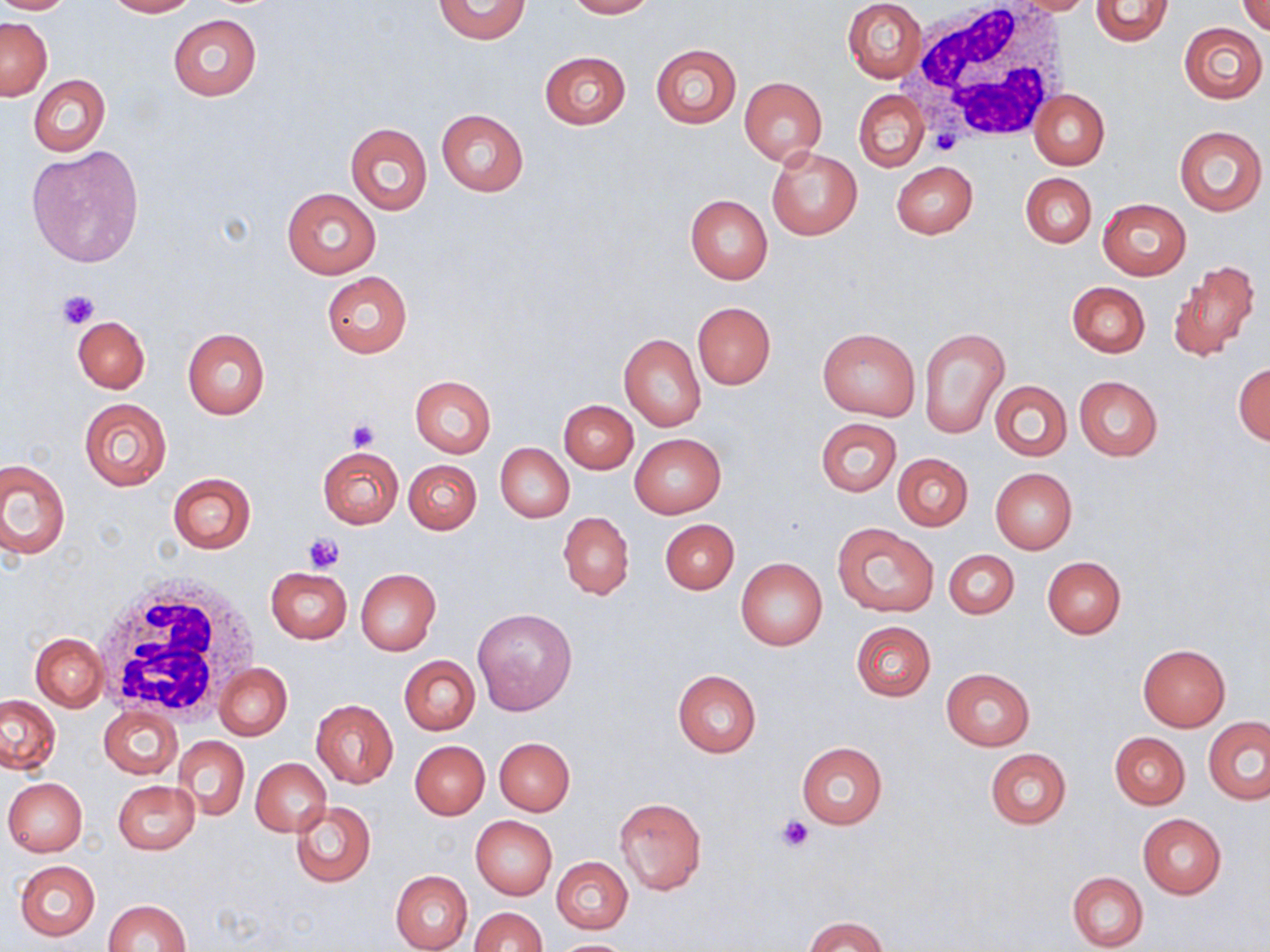
{
  "slide_level_diagnosis": "no evidence of blood parasites",
  "stain": "May-Grünwald-Giemsa",
  "preparation": "thin blood film",
  "image_size": "1270×952 pixels",
  "magnification": "1000x",
  "white_blood_cell_locations": "approximate bounding boxes as named x1/y1/x2/y2 corners in pixels: (x1=904, y1=3, x2=1075, y2=145), (x1=93, y1=575, x2=262, y2=725)",
  "uninfected_red_blood_cell_locations": "approximate bounding boxes as named x1/y1/x2/y2 corners in pixels: (x1=0, y1=0, x2=78, y2=14), (x1=104, y1=0, x2=197, y2=17), (x1=433, y1=0, x2=532, y2=44), (x1=564, y1=0, x2=654, y2=18), (x1=1001, y1=0, x2=1098, y2=15), (x1=843, y1=1, x2=926, y2=82), (x1=1089, y1=1, x2=1174, y2=47), (x1=1237, y1=1, x2=1270, y2=35), (x1=168, y1=14, x2=262, y2=101), (x1=1, y1=17, x2=52, y2=99), (x1=1179, y1=23, x2=1267, y2=103), (x1=650, y1=44, x2=741, y2=128), (x1=540, y1=51, x2=631, y2=129), (x1=28, y1=75, x2=110, y2=156), (x1=738, y1=77, x2=826, y2=166), (x1=854, y1=90, x2=929, y2=172), (x1=1030, y1=90, x2=1109, y2=170), (x1=1027, y1=91, x2=1100, y2=250), (x1=435, y1=109, x2=529, y2=196), (x1=344, y1=121, x2=432, y2=216), (x1=1173, y1=124, x2=1266, y2=216), (x1=26, y1=145, x2=144, y2=268), (x1=767, y1=147, x2=862, y2=240), (x1=891, y1=161, x2=977, y2=239), (x1=1020, y1=172, x2=1096, y2=249), (x1=281, y1=187, x2=381, y2=279), (x1=685, y1=195, x2=773, y2=284), (x1=1098, y1=198, x2=1191, y2=279), (x1=1170, y1=260, x2=1261, y2=361), (x1=321, y1=272, x2=413, y2=358), (x1=1067, y1=282, x2=1150, y2=357), (x1=693, y1=302, x2=775, y2=389), (x1=72, y1=316, x2=150, y2=393), (x1=182, y1=328, x2=270, y2=419), (x1=817, y1=328, x2=920, y2=420), (x1=920, y1=328, x2=1009, y2=437), (x1=619, y1=333, x2=706, y2=431), (x1=1233, y1=363, x2=1270, y2=445), (x1=410, y1=375, x2=496, y2=457), (x1=1074, y1=376, x2=1163, y2=461), (x1=989, y1=380, x2=1072, y2=462), (x1=78, y1=399, x2=172, y2=491), (x1=560, y1=400, x2=638, y2=473), (x1=816, y1=417, x2=901, y2=497), (x1=630, y1=434, x2=726, y2=517), (x1=495, y1=443, x2=574, y2=522), (x1=317, y1=447, x2=403, y2=529), (x1=892, y1=452, x2=973, y2=532), (x1=1, y1=460, x2=69, y2=559), (x1=404, y1=460, x2=481, y2=534), (x1=990, y1=468, x2=1077, y2=553), (x1=167, y1=473, x2=256, y2=552), (x1=559, y1=512, x2=634, y2=599), (x1=660, y1=519, x2=739, y2=595), (x1=832, y1=522, x2=938, y2=617), (x1=944, y1=550, x2=1019, y2=620), (x1=1042, y1=556, x2=1126, y2=639), (x1=736, y1=557, x2=827, y2=650), (x1=265, y1=567, x2=351, y2=643), (x1=354, y1=568, x2=441, y2=655), (x1=472, y1=608, x2=578, y2=716), (x1=851, y1=621, x2=935, y2=701), (x1=31, y1=632, x2=108, y2=711), (x1=1138, y1=643, x2=1230, y2=731), (x1=399, y1=655, x2=480, y2=735), (x1=214, y1=663, x2=292, y2=740), (x1=940, y1=667, x2=1035, y2=750), (x1=673, y1=669, x2=761, y2=757), (x1=0, y1=695, x2=61, y2=774), (x1=311, y1=699, x2=397, y2=788), (x1=99, y1=705, x2=182, y2=780), (x1=1205, y1=718, x2=1270, y2=804), (x1=1109, y1=731, x2=1190, y2=809), (x1=175, y1=736, x2=249, y2=821), (x1=495, y1=737, x2=575, y2=816), (x1=410, y1=741, x2=489, y2=820), (x1=795, y1=742, x2=888, y2=829), (x1=984, y1=748, x2=1072, y2=829), (x1=250, y1=758, x2=330, y2=836), (x1=3, y1=777, x2=87, y2=857), (x1=113, y1=780, x2=200, y2=855), (x1=613, y1=796, x2=707, y2=895), (x1=291, y1=801, x2=376, y2=887), (x1=1137, y1=813, x2=1226, y2=899), (x1=470, y1=816, x2=556, y2=900), (x1=552, y1=857, x2=632, y2=932), (x1=14, y1=860, x2=101, y2=940), (x1=391, y1=870, x2=472, y2=952), (x1=1066, y1=872, x2=1148, y2=951), (x1=103, y1=899, x2=191, y2=952), (x1=471, y1=906, x2=546, y2=952), (x1=804, y1=916, x2=886, y2=952), (x1=551, y1=938, x2=636, y2=951)",
  "field_of_view": "one of a larger specimen",
  "platelet_locations": "approximate bounding boxes as named x1/y1/x2/y2 corners in pixels: (x1=56, y1=289, x2=100, y2=330), (x1=344, y1=418, x2=380, y2=450), (x1=304, y1=534, x2=343, y2=574), (x1=775, y1=814, x2=815, y2=852)",
  "modality": "light microscopy"
}